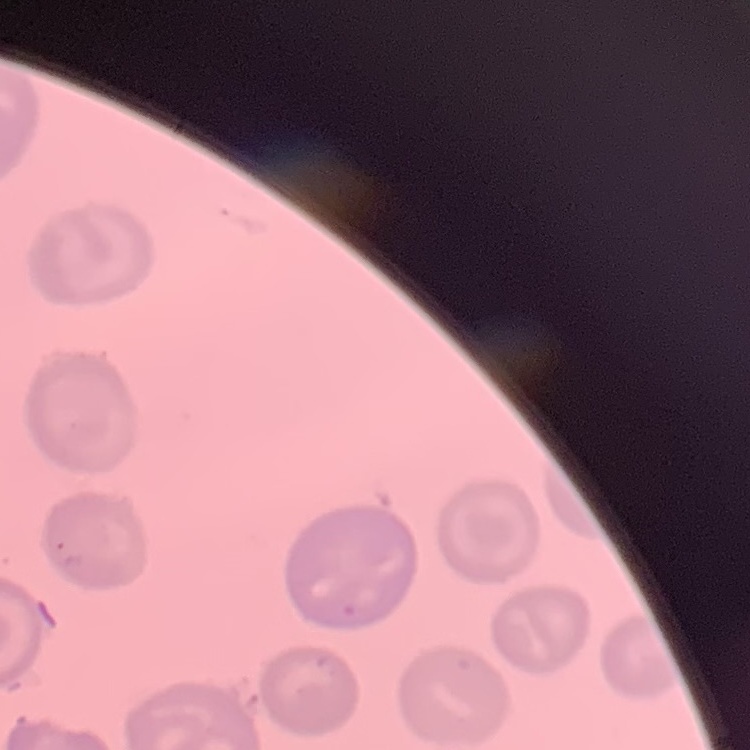
red blood cell morphology = no rouleaux formation
image type = one tile cut from a larger photomicrograph
stain = Field's or Giemsa
preparation = thin blood smear